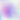

Toxoplasma gondii is seen. 400x magnification. Photomicrograph.